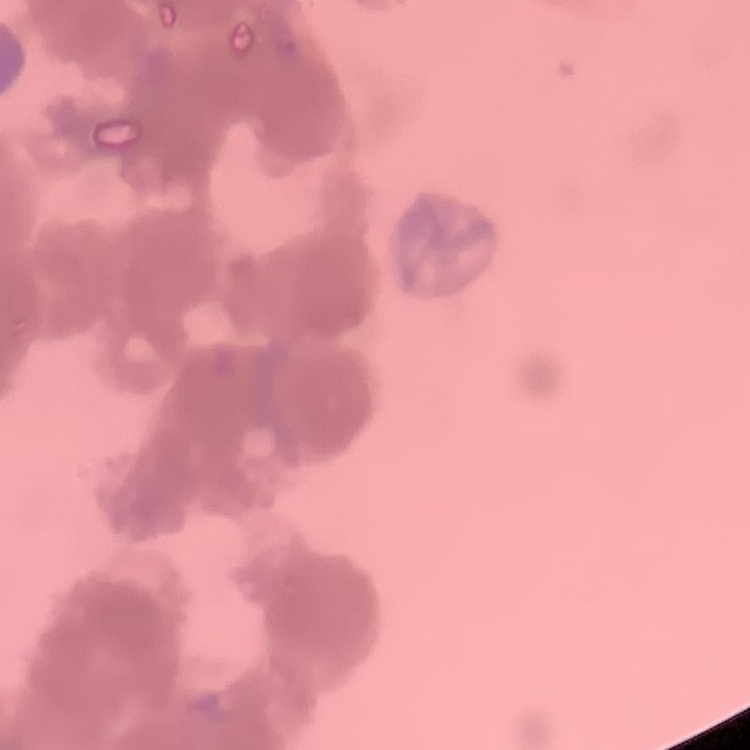

The erythrocytes exhibit rouleaux formation. Stained with either Field's or Giemsa. Square crop of a larger photomicrograph. Thin peripheral smear.